Identify the blood parasite species.
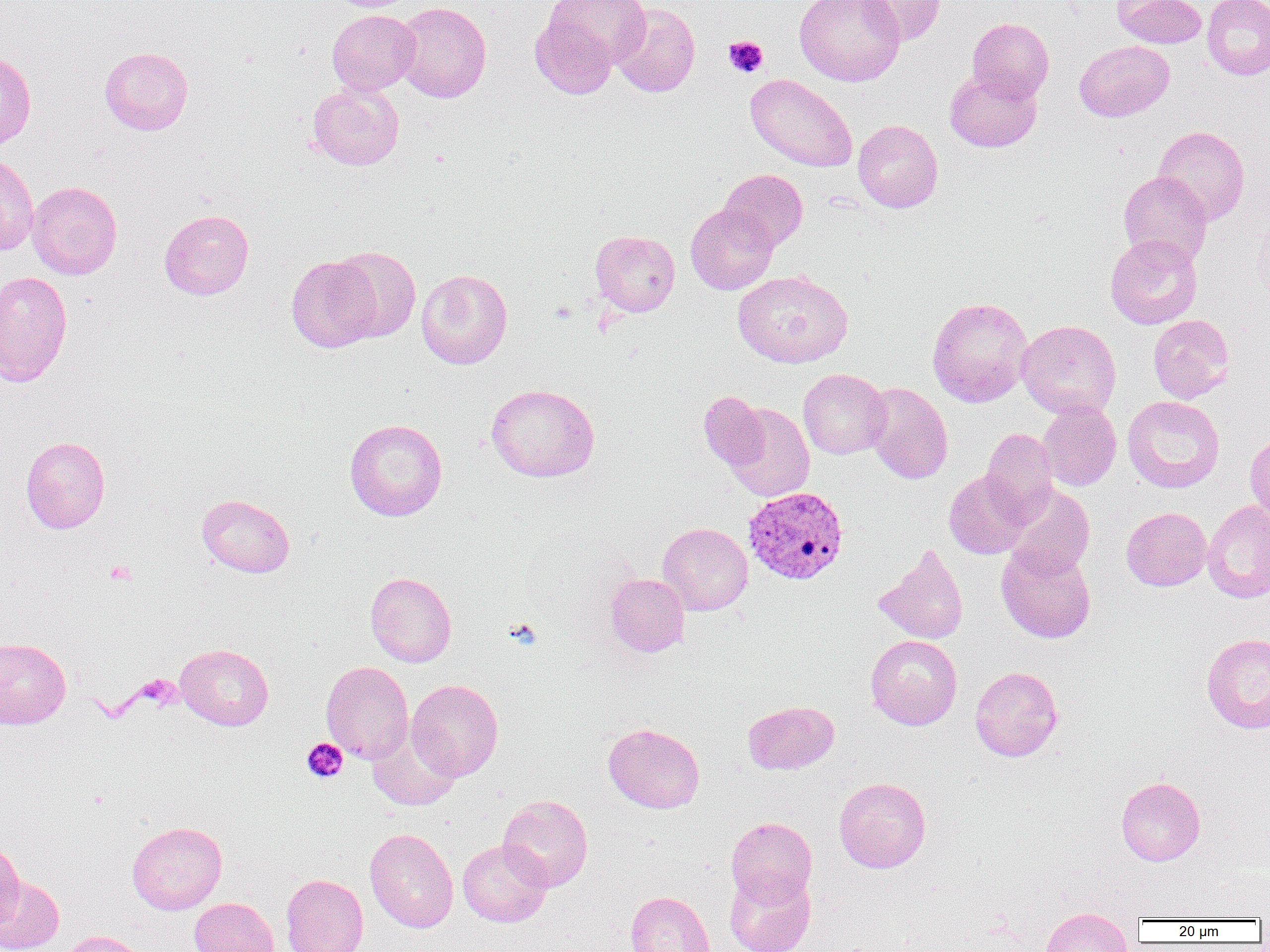
Plasmodium vivax.

Approximate bounding boxes as named x1/y1/x2/y2 corners in pixels. Uninfected red blood cell locations: (x1=545, y1=0, x2=650, y2=67), (x1=795, y1=0, x2=905, y2=86), (x1=857, y1=0, x2=946, y2=45), (x1=1113, y1=0, x2=1207, y2=49), (x1=1202, y1=0, x2=1270, y2=80), (x1=393, y1=1, x2=491, y2=103), (x1=611, y1=3, x2=701, y2=97), (x1=327, y1=10, x2=421, y2=95), (x1=529, y1=12, x2=618, y2=99), (x1=967, y1=18, x2=1054, y2=103), (x1=1074, y1=40, x2=1174, y2=122), (x1=99, y1=46, x2=193, y2=135), (x1=0, y1=51, x2=36, y2=150), (x1=945, y1=69, x2=1042, y2=152), (x1=745, y1=73, x2=858, y2=173), (x1=307, y1=82, x2=404, y2=170), (x1=853, y1=119, x2=943, y2=213), (x1=1154, y1=126, x2=1250, y2=224), (x1=0, y1=153, x2=39, y2=256), (x1=719, y1=169, x2=807, y2=251), (x1=1119, y1=171, x2=1212, y2=267), (x1=27, y1=181, x2=122, y2=280), (x1=685, y1=203, x2=779, y2=295), (x1=159, y1=208, x2=254, y2=299), (x1=590, y1=230, x2=680, y2=316), (x1=1105, y1=234, x2=1202, y2=329), (x1=329, y1=246, x2=421, y2=341), (x1=286, y1=255, x2=382, y2=352), (x1=416, y1=268, x2=512, y2=369), (x1=732, y1=269, x2=853, y2=368), (x1=0, y1=271, x2=73, y2=387), (x1=927, y1=296, x2=1033, y2=406), (x1=1148, y1=314, x2=1235, y2=403), (x1=1017, y1=319, x2=1121, y2=419), (x1=798, y1=369, x2=890, y2=459), (x1=863, y1=382, x2=953, y2=484), (x1=486, y1=383, x2=600, y2=482), (x1=699, y1=391, x2=769, y2=471), (x1=1123, y1=396, x2=1224, y2=492), (x1=1038, y1=400, x2=1122, y2=491), (x1=724, y1=403, x2=815, y2=502), (x1=344, y1=418, x2=447, y2=521), (x1=982, y1=427, x2=1057, y2=520), (x1=1245, y1=430, x2=1270, y2=528), (x1=21, y1=436, x2=110, y2=534), (x1=943, y1=469, x2=1032, y2=559), (x1=1005, y1=484, x2=1094, y2=577), (x1=196, y1=493, x2=295, y2=577), (x1=1202, y1=500, x2=1270, y2=602), (x1=1121, y1=507, x2=1211, y2=591), (x1=657, y1=522, x2=753, y2=615), (x1=996, y1=543, x2=1096, y2=643), (x1=874, y1=544, x2=969, y2=645), (x1=365, y1=572, x2=456, y2=667), (x1=605, y1=573, x2=689, y2=656), (x1=1202, y1=633, x2=1270, y2=733), (x1=866, y1=635, x2=962, y2=730), (x1=0, y1=637, x2=71, y2=729), (x1=175, y1=643, x2=274, y2=730), (x1=321, y1=661, x2=414, y2=763), (x1=970, y1=666, x2=1063, y2=761), (x1=406, y1=679, x2=503, y2=780), (x1=743, y1=700, x2=839, y2=774), (x1=603, y1=722, x2=705, y2=813), (x1=367, y1=726, x2=461, y2=811), (x1=1116, y1=776, x2=1205, y2=866), (x1=834, y1=777, x2=931, y2=873), (x1=498, y1=795, x2=593, y2=891), (x1=726, y1=816, x2=817, y2=906), (x1=127, y1=821, x2=227, y2=914), (x1=365, y1=828, x2=458, y2=932), (x1=458, y1=839, x2=552, y2=927), (x1=0, y1=841, x2=25, y2=930), (x1=724, y1=867, x2=816, y2=952), (x1=281, y1=874, x2=369, y2=952), (x1=0, y1=876, x2=64, y2=952), (x1=625, y1=890, x2=714, y2=952), (x1=189, y1=897, x2=279, y2=952), (x1=1040, y1=908, x2=1133, y2=952), (x1=58, y1=930, x2=152, y2=952). Plasmodium vivax-infected red blood cell locations: (x1=742, y1=486, x2=849, y2=586). Platelet locations: (x1=723, y1=35, x2=768, y2=78), (x1=550, y1=302, x2=577, y2=323), (x1=104, y1=560, x2=136, y2=585), (x1=505, y1=618, x2=542, y2=648), (x1=133, y1=675, x2=181, y2=711), (x1=301, y1=738, x2=348, y2=782). Optical microscopy. Image is 1270×952 pixels. Single field of view. Thin blood smear. Captured at 1000x magnification.